Assess this cell for malaria.
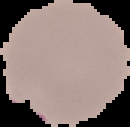

Parasitized.

preparation: thin blood film
image_size: 130×127 pixels
image_type: segmented cell region with the area outside set to black